State the blood parasite species.
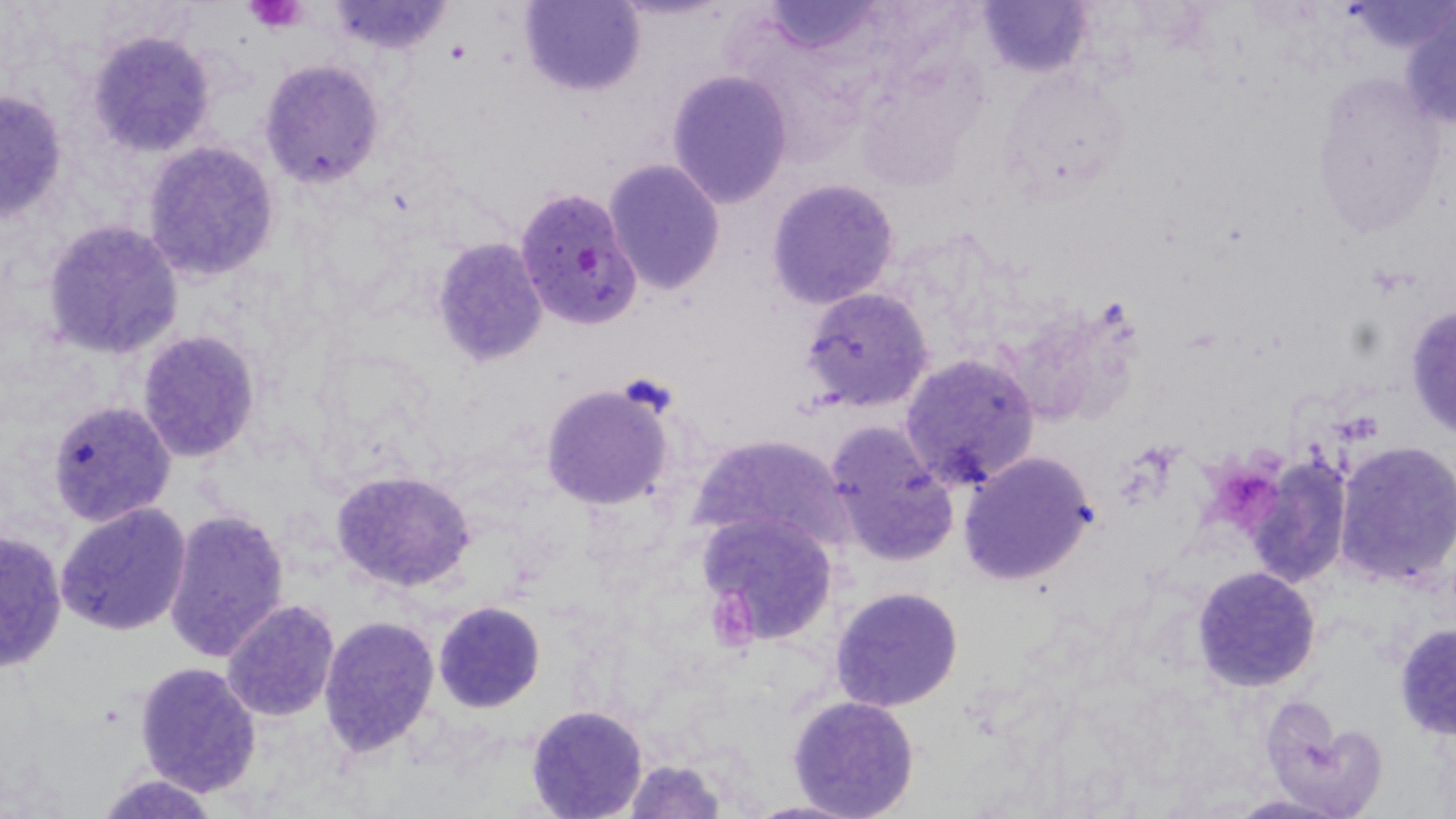
Plasmodium falciparum.

Summary:
  - Coordinate format: approximate bounding boxes as [x1, y1, x2, y2] in pixels
  - Plasmodium falciparum-infected red blood cell locations: [514, 186, 642, 331]
  - Uninfected red blood cell locations: [518, 0, 643, 98], [759, 1, 889, 57], [324, 2, 456, 54], [977, 2, 1090, 76], [1401, 5, 1456, 132], [86, 29, 217, 157], [259, 59, 386, 190], [998, 67, 1134, 201], [665, 70, 794, 208], [1310, 70, 1449, 239], [0, 89, 68, 223], [140, 141, 281, 282], [603, 158, 726, 295], [765, 178, 901, 308], [41, 219, 184, 360], [429, 236, 550, 367], [800, 286, 935, 412], [1403, 302, 1456, 439], [136, 329, 260, 463], [899, 352, 1040, 492], [536, 381, 679, 512], [46, 399, 177, 526], [825, 423, 959, 568], [689, 431, 854, 560], [1332, 441, 1456, 589], [955, 449, 1100, 586], [1245, 454, 1352, 590], [331, 468, 477, 595], [55, 501, 193, 636], [163, 508, 291, 663], [696, 510, 840, 646], [0, 528, 67, 674], [1192, 565, 1322, 691], [830, 586, 964, 712], [222, 599, 341, 721], [433, 601, 545, 713], [318, 615, 441, 755], [1393, 623, 1456, 740], [133, 659, 263, 796], [787, 695, 921, 818], [1260, 701, 1381, 815], [525, 705, 650, 819], [620, 758, 727, 819], [98, 773, 220, 817], [1227, 794, 1351, 818], [742, 799, 867, 819]
  - Platelet locations: [246, 1, 311, 31], [1212, 458, 1282, 529]
  - Preparation: thin blood film
  - Image size: 1456×819 pixels
  - Field of view: single
  - Modality: optical microscopy
  - Stain: May-Grünwald-Giemsa
  - Magnification: 1000x